Name the parasite shown.
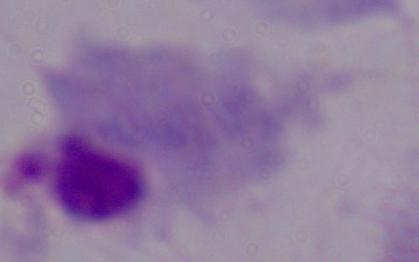

This is a trichomonad.

Micrograph. Captured at 1000x magnification.